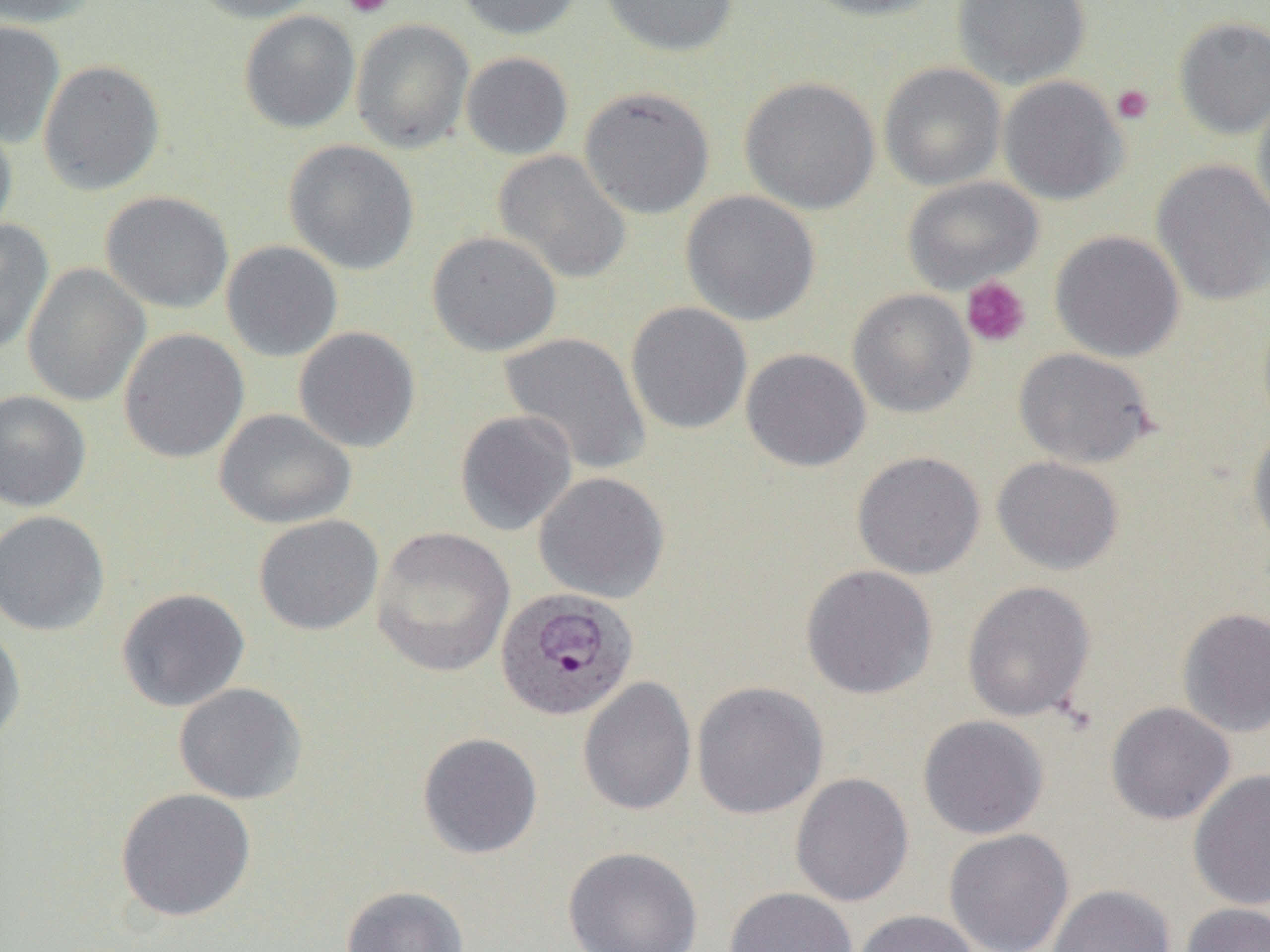
Summary:
  - Coordinate format: approximate bounding boxes as named x1/y1/x2/y2 corners in pixels
  - Plasmodium ovale-infected red blood cell locations: (x1=495, y1=587, x2=639, y2=722)
  - Platelet locations: (x1=342, y1=0, x2=393, y2=19), (x1=1111, y1=83, x2=1155, y2=125), (x1=961, y1=276, x2=1031, y2=349)
  - Uninfected red blood cell locations: (x1=0, y1=0, x2=99, y2=27), (x1=187, y1=0, x2=327, y2=23), (x1=455, y1=0, x2=585, y2=40), (x1=600, y1=0, x2=739, y2=58), (x1=798, y1=0, x2=949, y2=21), (x1=952, y1=0, x2=1091, y2=88), (x1=239, y1=10, x2=360, y2=133), (x1=1173, y1=16, x2=1270, y2=138), (x1=350, y1=18, x2=474, y2=153), (x1=0, y1=20, x2=65, y2=149), (x1=460, y1=52, x2=574, y2=160), (x1=38, y1=60, x2=165, y2=196), (x1=878, y1=62, x2=1006, y2=191), (x1=998, y1=75, x2=1128, y2=205), (x1=739, y1=76, x2=880, y2=215), (x1=578, y1=86, x2=715, y2=219), (x1=1252, y1=92, x2=1270, y2=229), (x1=0, y1=114, x2=17, y2=244), (x1=283, y1=140, x2=420, y2=275), (x1=492, y1=150, x2=632, y2=285), (x1=1151, y1=159, x2=1270, y2=307), (x1=902, y1=176, x2=1044, y2=294), (x1=100, y1=190, x2=234, y2=314), (x1=681, y1=190, x2=821, y2=326), (x1=0, y1=219, x2=54, y2=356), (x1=427, y1=230, x2=563, y2=357), (x1=1050, y1=230, x2=1185, y2=362), (x1=221, y1=240, x2=343, y2=362), (x1=23, y1=262, x2=150, y2=407), (x1=847, y1=288, x2=977, y2=418), (x1=625, y1=301, x2=753, y2=435), (x1=293, y1=326, x2=421, y2=453), (x1=118, y1=328, x2=249, y2=463), (x1=498, y1=331, x2=651, y2=475), (x1=740, y1=348, x2=871, y2=472), (x1=1013, y1=348, x2=1157, y2=468), (x1=0, y1=389, x2=91, y2=512), (x1=214, y1=408, x2=357, y2=529), (x1=454, y1=409, x2=578, y2=536), (x1=1247, y1=424, x2=1270, y2=553), (x1=852, y1=451, x2=986, y2=579), (x1=991, y1=455, x2=1124, y2=575), (x1=533, y1=471, x2=670, y2=603), (x1=0, y1=510, x2=110, y2=636), (x1=253, y1=514, x2=384, y2=635), (x1=371, y1=527, x2=516, y2=678), (x1=800, y1=564, x2=938, y2=699), (x1=962, y1=580, x2=1095, y2=722), (x1=116, y1=587, x2=250, y2=712), (x1=1176, y1=606, x2=1270, y2=738), (x1=0, y1=622, x2=27, y2=750), (x1=578, y1=676, x2=697, y2=817), (x1=691, y1=681, x2=829, y2=820), (x1=174, y1=683, x2=307, y2=805), (x1=1105, y1=701, x2=1236, y2=825), (x1=917, y1=715, x2=1049, y2=839), (x1=417, y1=732, x2=543, y2=859), (x1=1188, y1=769, x2=1270, y2=911), (x1=789, y1=772, x2=914, y2=907), (x1=115, y1=788, x2=256, y2=922), (x1=943, y1=828, x2=1074, y2=952), (x1=563, y1=846, x2=703, y2=952), (x1=1047, y1=884, x2=1176, y2=952), (x1=340, y1=885, x2=470, y2=952), (x1=724, y1=886, x2=858, y2=952), (x1=1180, y1=903, x2=1270, y2=952), (x1=852, y1=909, x2=981, y2=952)
  - Slide-level diagnosis: Plasmodium ovale
  - Image size: 1270×952 pixels
  - Preparation: thin blood film
  - Magnification: 1000x
  - Modality: optical microscopy
  - Field of view: one of a larger specimen